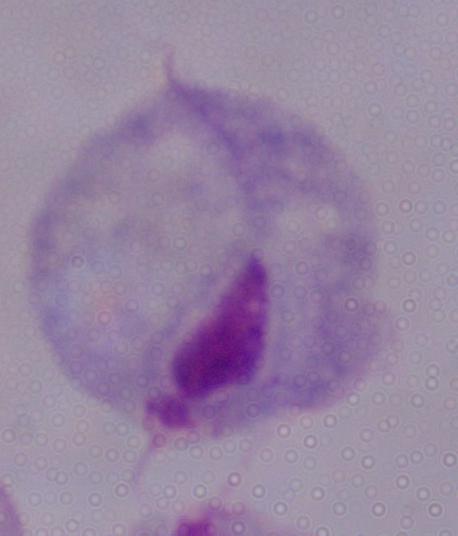 A trichomonad is shown. Micrograph. Captured at 1000x magnification.